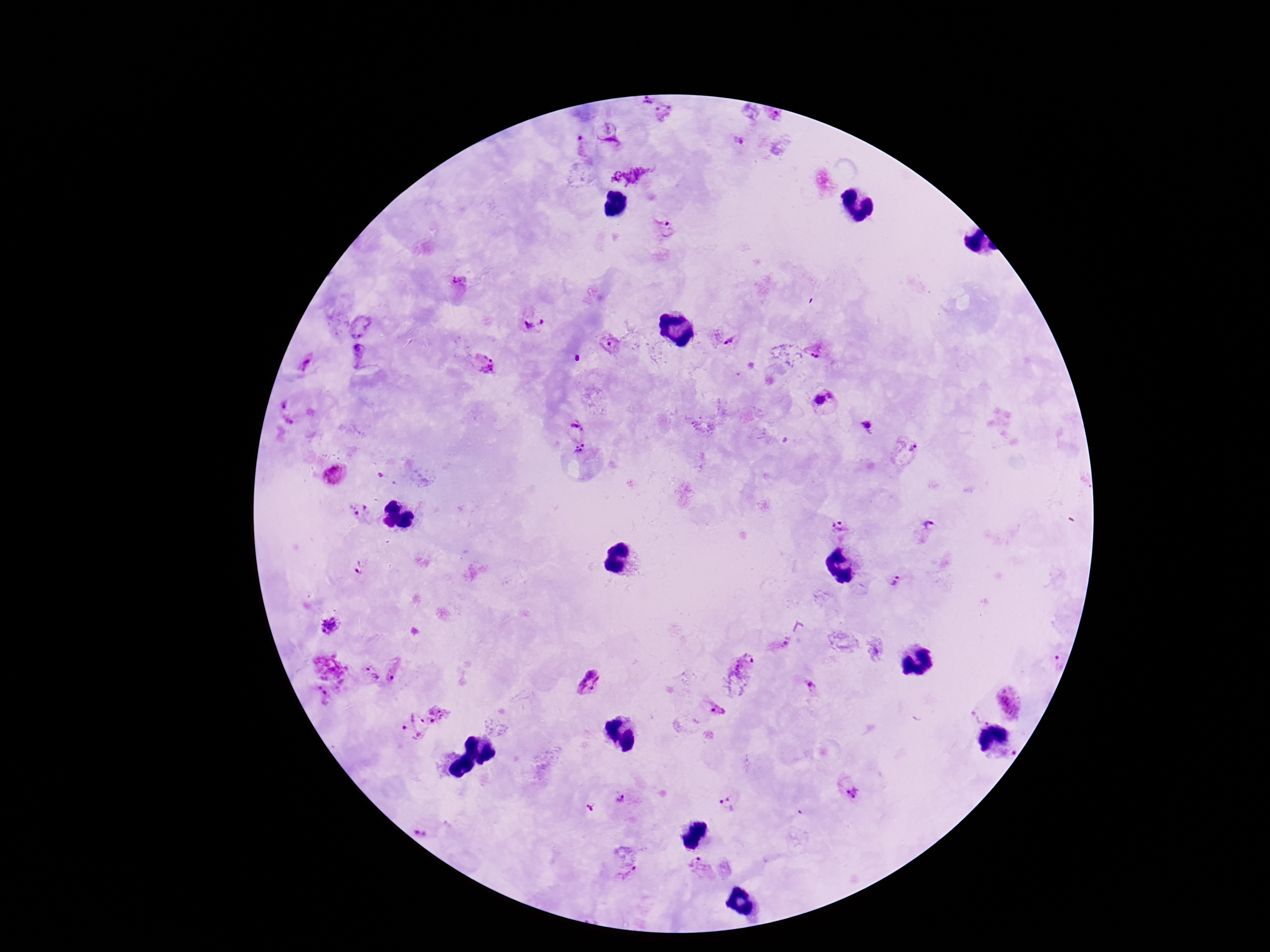
Approximate object centers, in pixels from the top-left corner. Plasmodium parasite locations: (x=644, y=101), (x=663, y=113), (x=774, y=118), (x=608, y=131), (x=736, y=141), (x=580, y=147), (x=664, y=231), (x=460, y=286), (x=530, y=322), (x=360, y=326), (x=724, y=336), (x=817, y=344), (x=611, y=348), (x=358, y=354), (x=482, y=364), (x=305, y=365), (x=826, y=402), (x=290, y=411), (x=705, y=428), (x=574, y=429), (x=865, y=429), (x=906, y=449), (x=586, y=454), (x=335, y=473), (x=359, y=512), (x=926, y=531), (x=841, y=532), (x=362, y=569), (x=898, y=578), (x=329, y=626), (x=780, y=646), (x=742, y=666), (x=397, y=672), (x=369, y=674), (x=589, y=683), (x=811, y=687), (x=320, y=697), (x=1007, y=702), (x=716, y=711), (x=981, y=715), (x=419, y=718), (x=849, y=788), (x=622, y=801), (x=730, y=804), (x=586, y=810), (x=428, y=830), (x=701, y=867), (x=628, y=873). Giemsa stain. Thick peripheral-blood smear. Image is 1270×952 pixels. Single field of view. Patient malaria status: infected. 100x magnification. Smartphone photograph taken through the microscope eyepiece.